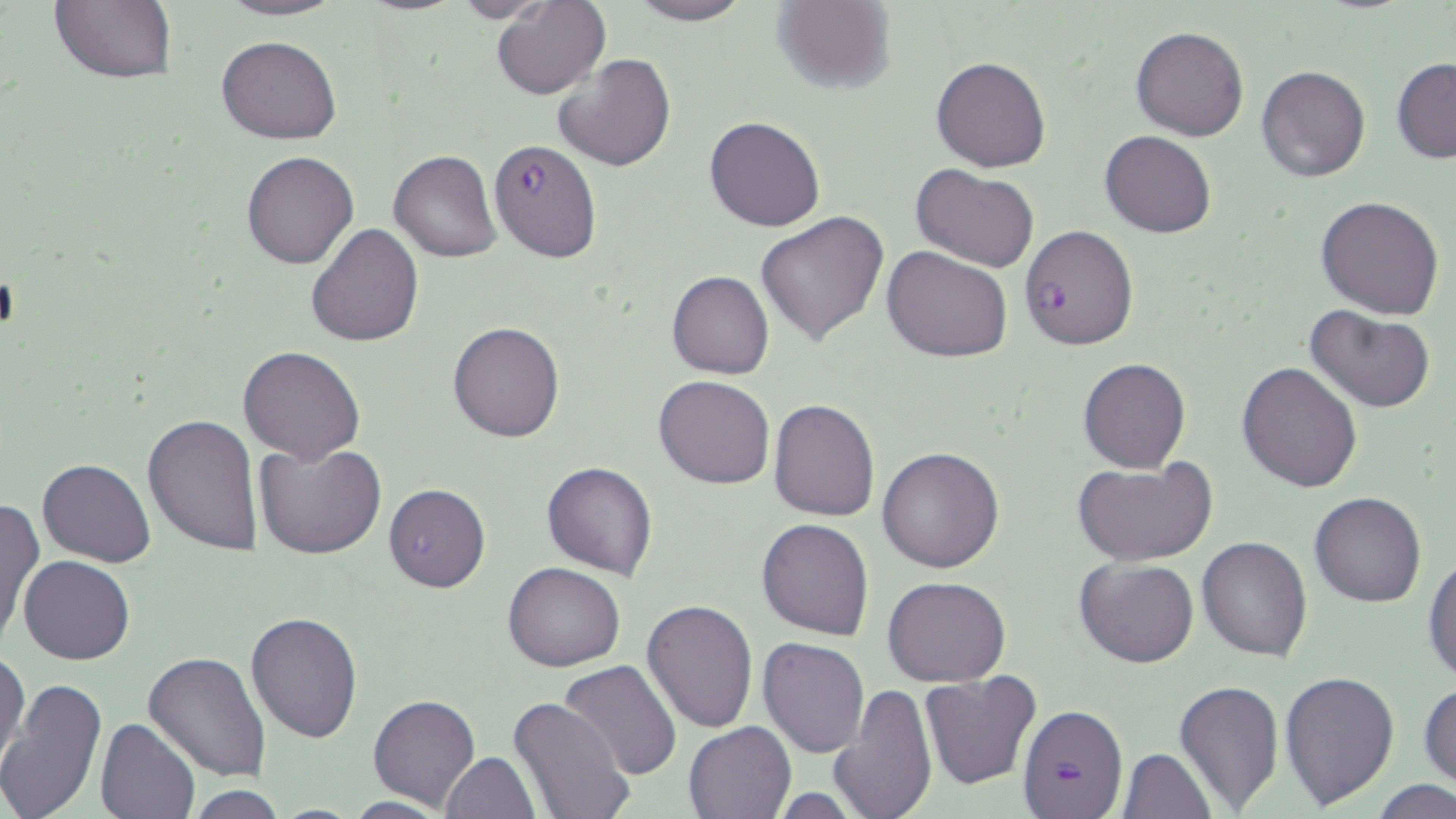
Approximate bounding boxes as (x1,y1)-(x2,y2) corner pairs in pixels. Plasmodium falciparum-infected red blood cell locations: (488,138)-(601,263), (1017,223)-(1139,351), (1020,705)-(1128,819). Platelet locations: (0,273)-(19,332). Uninfected red blood cell locations: (48,0)-(178,86), (216,0)-(347,21), (492,0)-(609,100), (624,0)-(752,25), (772,0)-(897,93), (447,1)-(556,22), (1131,25)-(1249,142), (216,35)-(342,145), (552,53)-(676,173), (931,56)-(1051,172), (1391,58)-(1456,164), (1257,65)-(1370,182), (704,115)-(825,232), (1100,131)-(1217,238), (389,149)-(502,263), (240,150)-(359,270), (910,164)-(1040,273), (1314,196)-(1445,319), (756,210)-(890,347), (305,223)-(424,347), (882,245)-(1014,363), (667,270)-(774,378), (1304,307)-(1437,414), (448,321)-(564,442), (238,344)-(366,465), (1077,356)-(1191,474), (1236,361)-(1363,493), (653,375)-(775,489), (767,399)-(881,521), (141,413)-(263,555), (253,441)-(387,560), (877,446)-(1005,574), (36,458)-(157,567), (541,461)-(659,580), (1073,461)-(1215,567), (383,483)-(491,593), (1308,493)-(1428,607), (1,498)-(42,648), (757,518)-(874,641), (1196,535)-(1314,660), (1423,553)-(1456,686), (19,556)-(134,666), (1075,557)-(1200,669), (503,562)-(626,672), (882,574)-(1013,687), (641,600)-(760,734), (245,610)-(363,743), (757,637)-(869,757), (143,650)-(272,781), (1,652)-(30,774), (556,660)-(682,781), (918,670)-(1041,791), (1279,671)-(1401,809), (0,676)-(106,819), (1174,680)-(1284,809), (831,683)-(938,819), (1418,684)-(1455,791), (365,693)-(481,809), (506,697)-(633,819), (97,717)-(200,819), (683,720)-(798,818), (1119,748)-(1216,819), (440,752)-(539,818), (1372,780)-(1455,818), (182,787)-(295,819). Slide-level diagnosis: Plasmodium falciparum. Image is 1456×819 pixels. Thin blood smear. May-Grünwald-Giemsa stain. Single field of view. 1000x magnification. Optical microscopy.